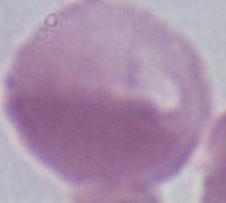
modality = micrograph
identification = red blood cell
magnification = 1000x